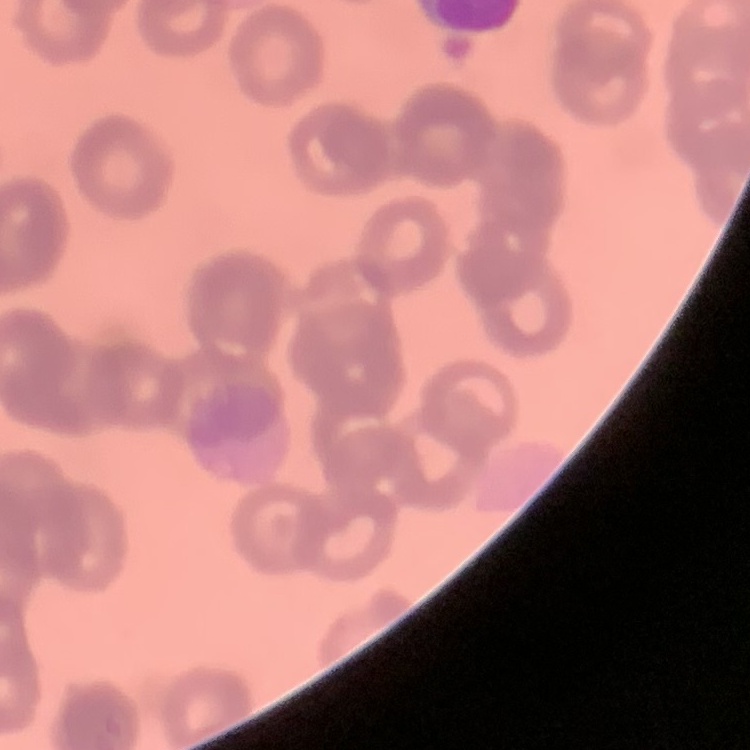
Summary:
  - Erythrocyte morphology: rouleaux formation
  - Image type: square crop of a larger photomicrograph
  - Stain: Field's or Giemsa
  - Preparation: thin peripheral smear